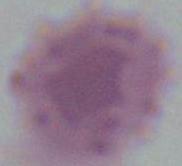
Summary:
  - Modality: photomicrograph
  - Identification: erythrocyte
  - Magnification: 1000x